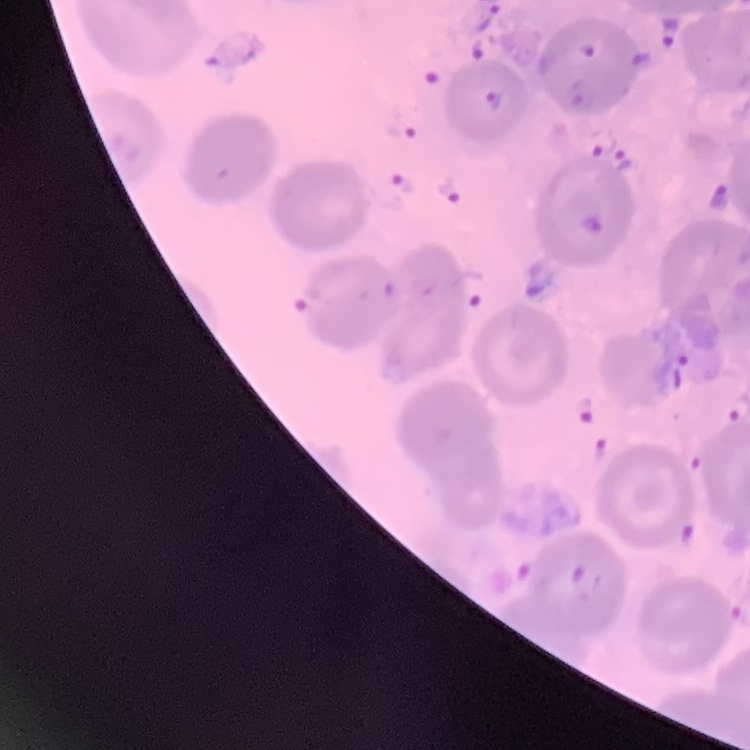
erythrocyte morphology = no rouleaux formation
preparation = thin peripheral smear
image type = one tile cut from a larger photomicrograph
stain = Field's or Giemsa